Report the malaria status of this cell.
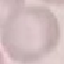

It is uninfected.

Thin smear of blood. Giemsa stain. Automatically extracted cell patch, resized to 64 × 64 pixels. Photographed with a smartphone camera at the microscope eyepiece.